Give the position of every leukocyte visible.
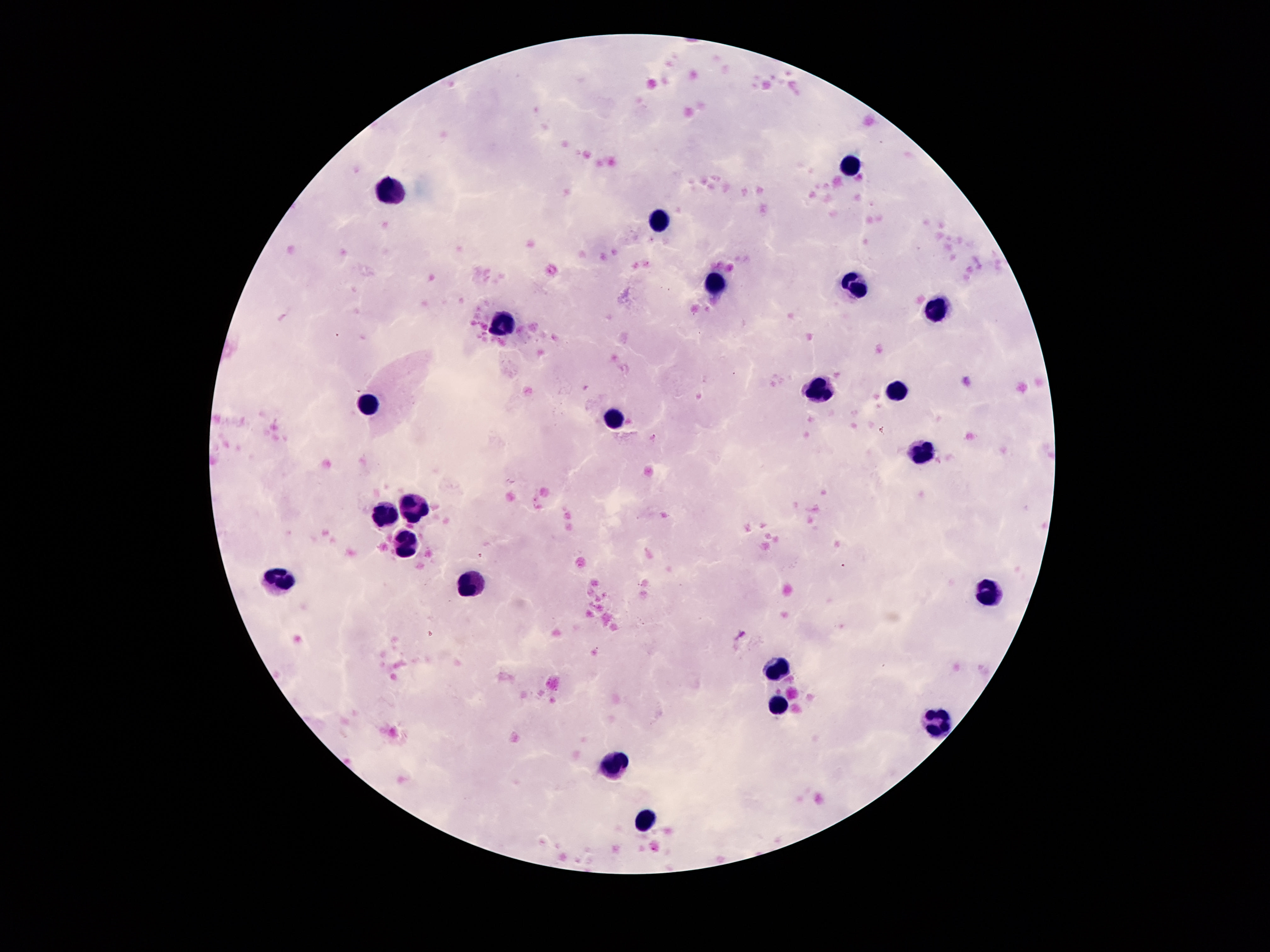

Approximate centers as [x, y] in pixels.
Leukocytes: [853, 166], [386, 188], [658, 221], [714, 285], [851, 285], [931, 310], [506, 325], [897, 387], [820, 393], [371, 404], [612, 417], [920, 449], [417, 504], [382, 513], [409, 542], [278, 583], [470, 590], [986, 590], [776, 668], [778, 705], [935, 718], [616, 764], [643, 822].

capture = smartphone camera through the microscope eyepiece
image size = 1270×952 pixels
stain = Giemsa
field of view = one from this slide
preparation = thick blood smear
patient malaria status = not infected
magnification = 100x